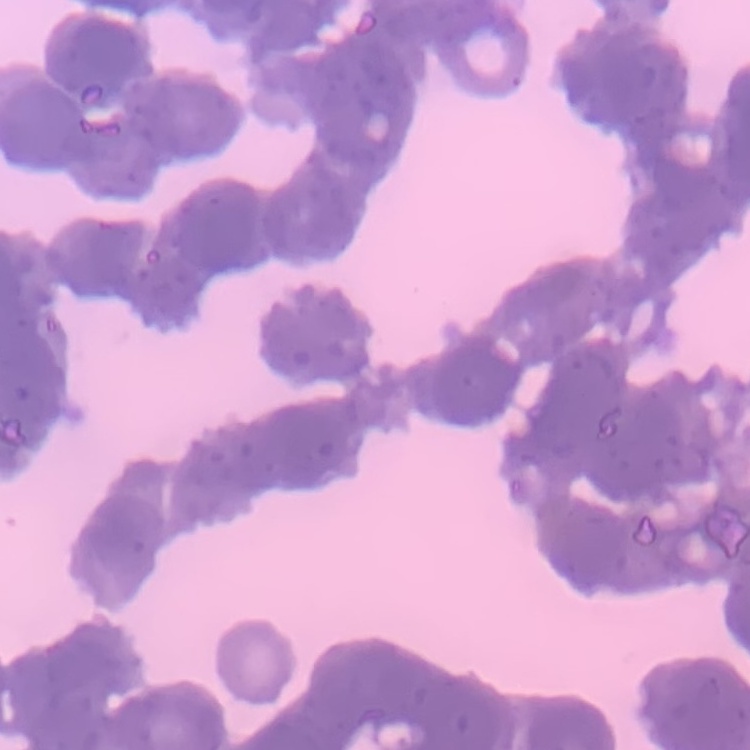

The red blood cells exhibit rouleaux formation. Field's or Giemsa stain. Square crop of a larger photomicrograph. Thin blood smear.